Give the position of every Plasmodium parasite.
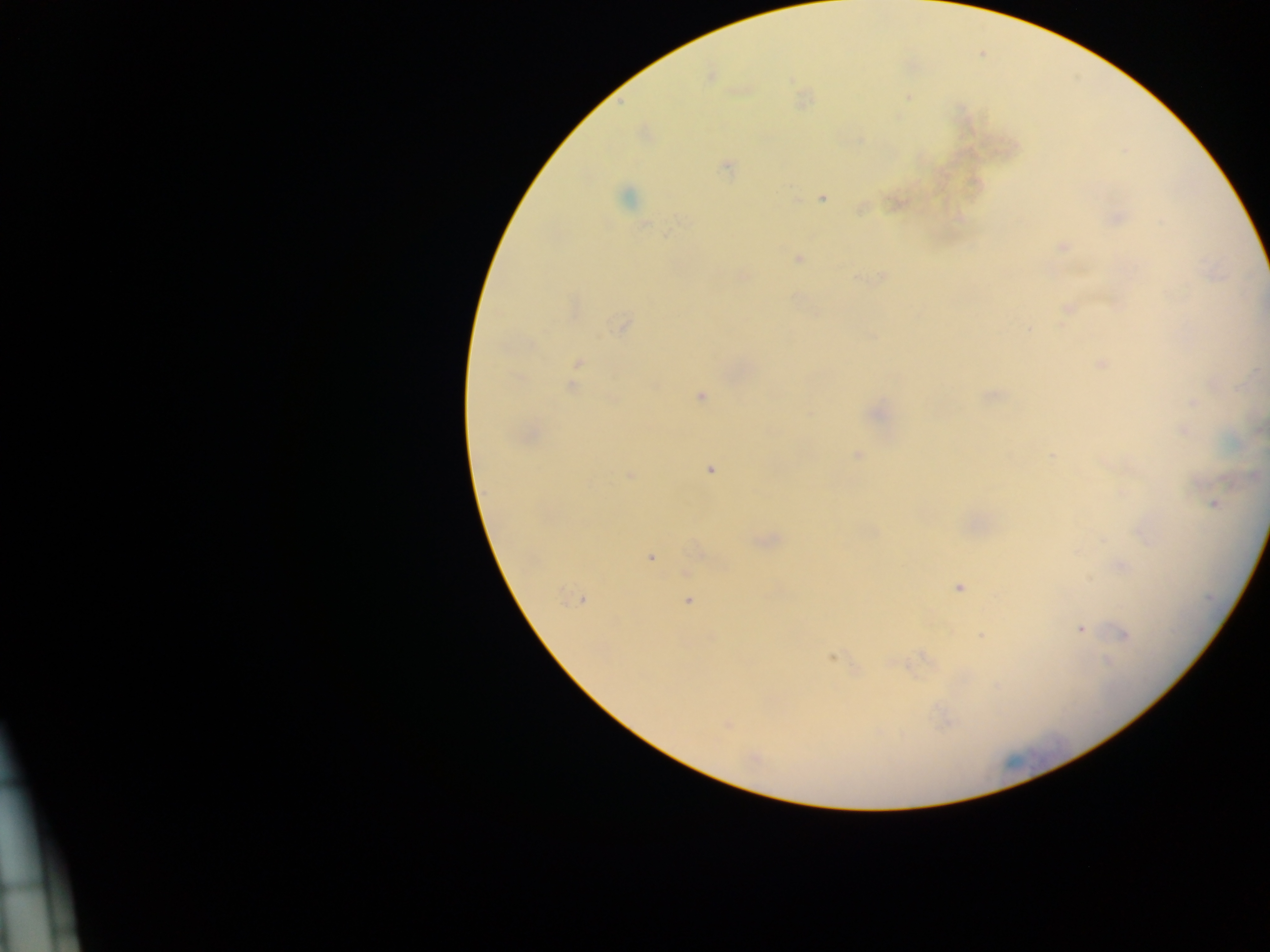

Approximate centers as [x, y] in pixels.
Plasmodium parasites: [710, 74], [740, 90], [907, 98], [803, 99], [727, 166], [627, 197], [821, 197], [896, 202], [861, 207], [1114, 217], [1062, 247], [798, 258], [742, 276], [882, 278], [1068, 309], [622, 324], [577, 363], [1101, 364], [571, 385], [991, 395], [700, 396], [1193, 403], [876, 412], [1183, 430], [527, 435], [857, 455], [1052, 455], [709, 469], [629, 475], [1213, 503], [1142, 531], [766, 539], [700, 551], [651, 557], [1120, 565], [958, 588], [577, 598], [688, 600], [1080, 628], [982, 635], [1124, 635], [831, 657], [726, 724], [754, 759].

Single field of view. Image is 1270×952 pixels. Mobile-phone photograph taken through the microscope. Sample from Ghana. Thick blood smear.